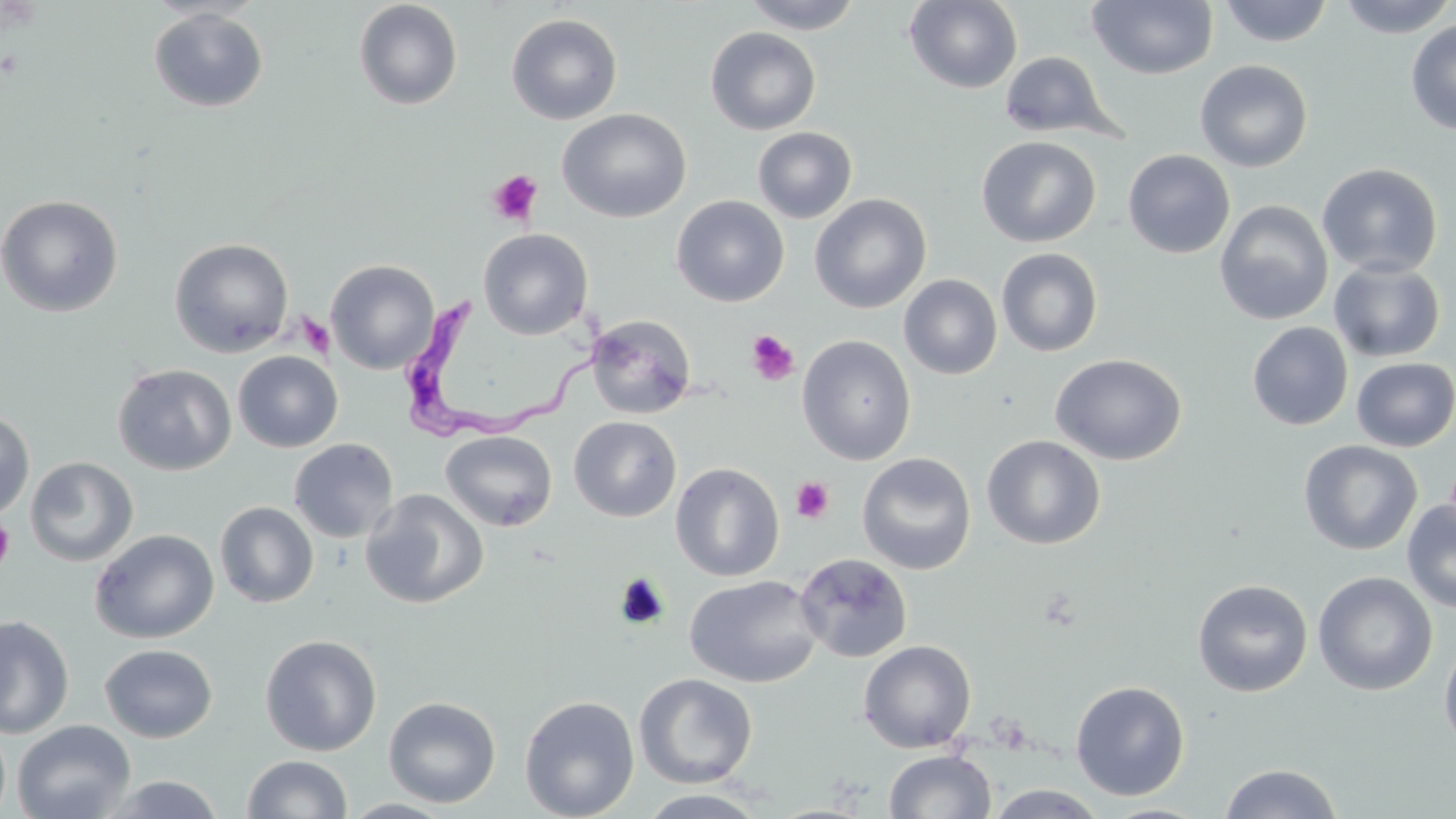 Approximate bounding boxes as (x1,y1)-(x2,y2) corner pairs in pixels. Trypanosoma brucei locations: (387,290)-(614,442). Platelet locations: (487,170)-(543,226), (296,313)-(334,358), (745,329)-(800,386), (790,476)-(835,524), (0,517)-(16,573). Uninfected red blood cell locations: (740,0)-(864,34), (904,0)-(1022,93), (1217,0)-(1334,47), (1336,0)-(1456,38), (353,1)-(463,110), (1087,1)-(1218,80), (148,7)-(269,112), (505,13)-(623,125), (1405,18)-(1456,136), (705,26)-(821,135), (998,51)-(1120,142), (1195,59)-(1313,172), (557,108)-(692,224), (752,126)-(857,223), (976,135)-(1101,248), (1122,149)-(1235,258), (1317,163)-(1443,278), (809,193)-(931,314), (0,195)-(123,317), (671,195)-(790,307), (1215,200)-(1333,325), (478,229)-(593,340), (169,238)-(295,358), (996,248)-(1103,357), (325,259)-(439,374), (1329,260)-(1446,363), (899,274)-(1003,380), (585,314)-(697,419), (1247,322)-(1353,431), (797,335)-(917,465), (233,351)-(343,452), (1050,353)-(1187,466), (1351,357)-(1456,451), (112,363)-(237,475), (0,409)-(35,520), (568,416)-(682,522), (440,430)-(557,531), (981,434)-(1106,550), (288,438)-(398,543), (1298,440)-(1423,555), (853,450)-(1103,564), (857,452)-(976,575), (25,456)-(138,566), (670,462)-(784,581), (360,489)-(489,609), (1402,499)-(1456,613), (214,501)-(319,608), (89,529)-(219,644), (793,552)-(913,663), (1313,571)-(1438,696), (684,574)-(822,688), (1192,579)-(1313,697), (0,614)-(75,739), (260,634)-(382,756), (1439,636)-(1456,756), (858,640)-(976,753), (99,643)-(218,743), (634,673)-(758,788), (1070,680)-(1190,800), (519,695)-(640,819), (383,696)-(501,808), (12,720)-(136,819), (884,749)-(996,819), (241,755)-(353,818), (1218,763)-(1344,819), (100,773)-(227,818), (982,785)-(1109,819), (636,788)-(770,818), (341,798)-(456,818), (1098,803)-(1212,819). Slide-level diagnosis: Trypanosoma brucei. Image is 1456×819 pixels. 1000x magnification. Light microscopy. May-Grünwald-Giemsa stain. One field of a larger specimen. Thin blood film.